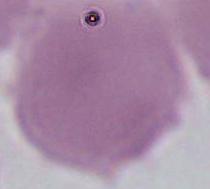

{
  "identification": "erythrocyte",
  "magnification": "1000x",
  "modality": "photomicrograph"
}